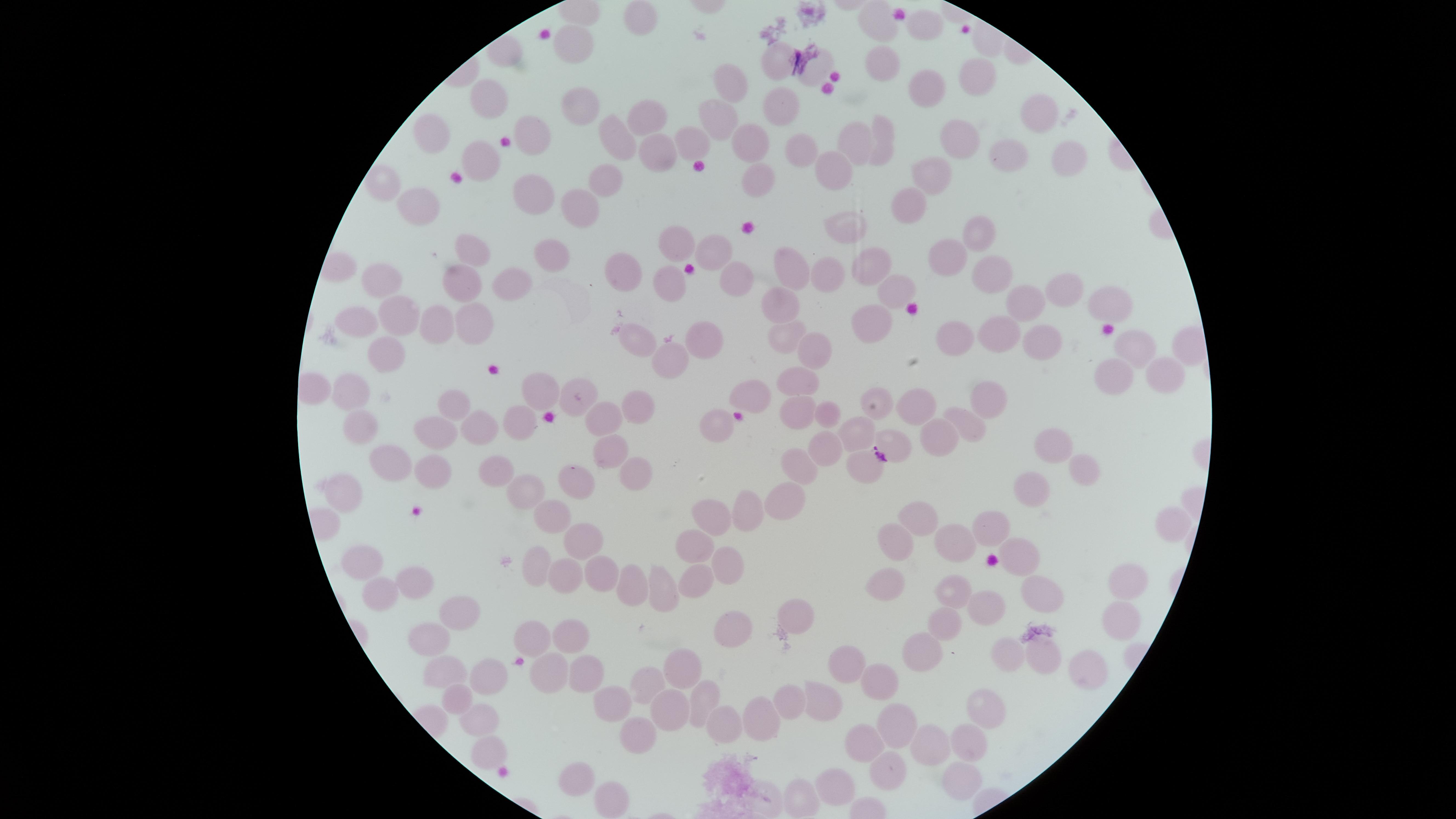

Approximate marker points as {x, y} in pixels. Uninfected RBCs: {636, 16}, {874, 20}, {926, 23}, {580, 43}, {882, 57}, {775, 58}, {814, 69}, {976, 70}, {733, 81}, {929, 90}, {493, 97}, {586, 107}, {779, 109}, {1040, 112}, {646, 116}, {717, 122}, {618, 135}, {532, 136}, {885, 138}, {434, 140}, {687, 141}, {859, 143}, {962, 143}, {750, 144}, {651, 149}, {801, 149}, {1067, 154}, {1008, 157}, {486, 160}, {831, 176}, {609, 178}, {932, 179}, {758, 186}, {384, 188}, {521, 190}, {571, 201}, {914, 201}, {416, 211}, {844, 235}, {976, 236}, {683, 247}, {714, 247}, {471, 254}, {548, 254}, {945, 256}, {871, 263}, {995, 269}, {829, 272}, {626, 273}, {790, 274}, {675, 280}, {734, 280}, {385, 281}, {464, 287}, {513, 289}, {895, 289}, {1055, 289}, {1104, 303}, {1026, 305}, {783, 308}, {399, 315}, {468, 315}, {364, 319}, {442, 319}, {875, 324}, {640, 333}, {788, 336}, {1001, 339}, {705, 341}, {955, 344}, {1041, 344}, {1130, 344}, {811, 350}, {388, 356}, {679, 363}, {1170, 374}, {802, 379}, {1107, 379}, {751, 387}, {537, 388}, {354, 395}, {579, 397}, {985, 398}, {456, 403}, {640, 405}, {879, 410}, {914, 410}, {831, 414}, {801, 415}, {614, 418}, {520, 419}, {712, 419}, {962, 422}, {363, 425}, {479, 426}, {853, 434}, {936, 435}, {438, 437}, {891, 442}, {1054, 446}, {821, 452}, {608, 453}, {389, 463}, {1085, 466}, {498, 468}, {799, 468}, {862, 468}, {430, 471}, {638, 472}, {347, 484}, {575, 485}, {1031, 485}, {522, 490}, {789, 505}, {749, 511}, {919, 518}, {711, 520}, {548, 523}, {1173, 524}, {992, 525}, {584, 540}, {955, 543}, {893, 544}, {696, 546}, {1026, 560}, {533, 562}, {364, 563}, {732, 568}, {573, 575}, {598, 577}, {693, 578}, {414, 584}, {889, 585}, {1122, 585}, {628, 586}, {1049, 586}, {654, 591}, {382, 592}, {951, 597}, {982, 613}, {458, 615}, {801, 617}, {1116, 619}, {946, 625}, {725, 628}, {529, 633}, {566, 635}, {435, 645}, {1009, 648}, {921, 656}, {1049, 656}, {683, 666}, {847, 666}, {1089, 669}, {547, 671}, {444, 675}, {581, 677}, {490, 678}, {877, 682}, {639, 685}, {786, 693}, {455, 696}, {701, 701}, {818, 703}, {610, 705}, {481, 709}, {669, 710}, {979, 712}, {764, 723}, {717, 725}, {902, 728}, {632, 737}, {931, 741}, {865, 743}, {967, 746}, {479, 757}, {886, 769}, {949, 777}, {579, 780}, {828, 788}, {801, 798}, {606, 800}, {761, 800}. Thin blood smear. The visible region is circular. Presence: no malaria parasites detected. Image is 1456×819 pixels. Giemsa-stained preparation. Photographed with a smartphone camera through the microscope eyepiece. One field of view of the specimen.